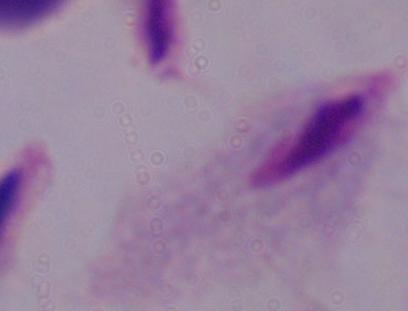

identification = trichomonad
magnification = 1000x
modality = photomicrograph